Classify this cell by malaria status.
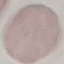
It is uninfected.

image type = automatically extracted cell patch, resized to 64 × 64 pixels
capture = smartphone camera at the microscope eyepiece
preparation = thin blood smear
stain = Giemsa